Name the cell type shown.
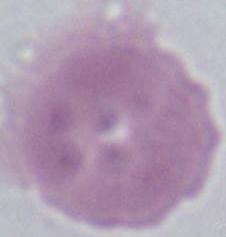
This is an erythrocyte.

modality = micrograph
magnification = 1000x